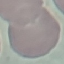
Summary:
  - Result: no malaria parasites seen
  - Stain: Giemsa
  - Capture: smartphone camera at the microscope eyepiece
  - Preparation: thin blood film
  - Image type: automatically extracted cell patch, resized to 64 × 64 pixels